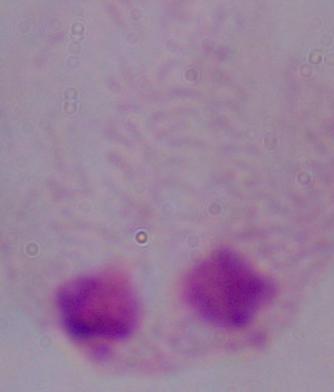
identification = trichomonad
modality = micrograph
magnification = 1000x